Classify this cell by malaria status.
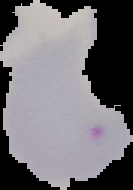
It is parasitized.

Image is 133×190 pixels. Segmented cell region on a black background. From a thin blood smear.